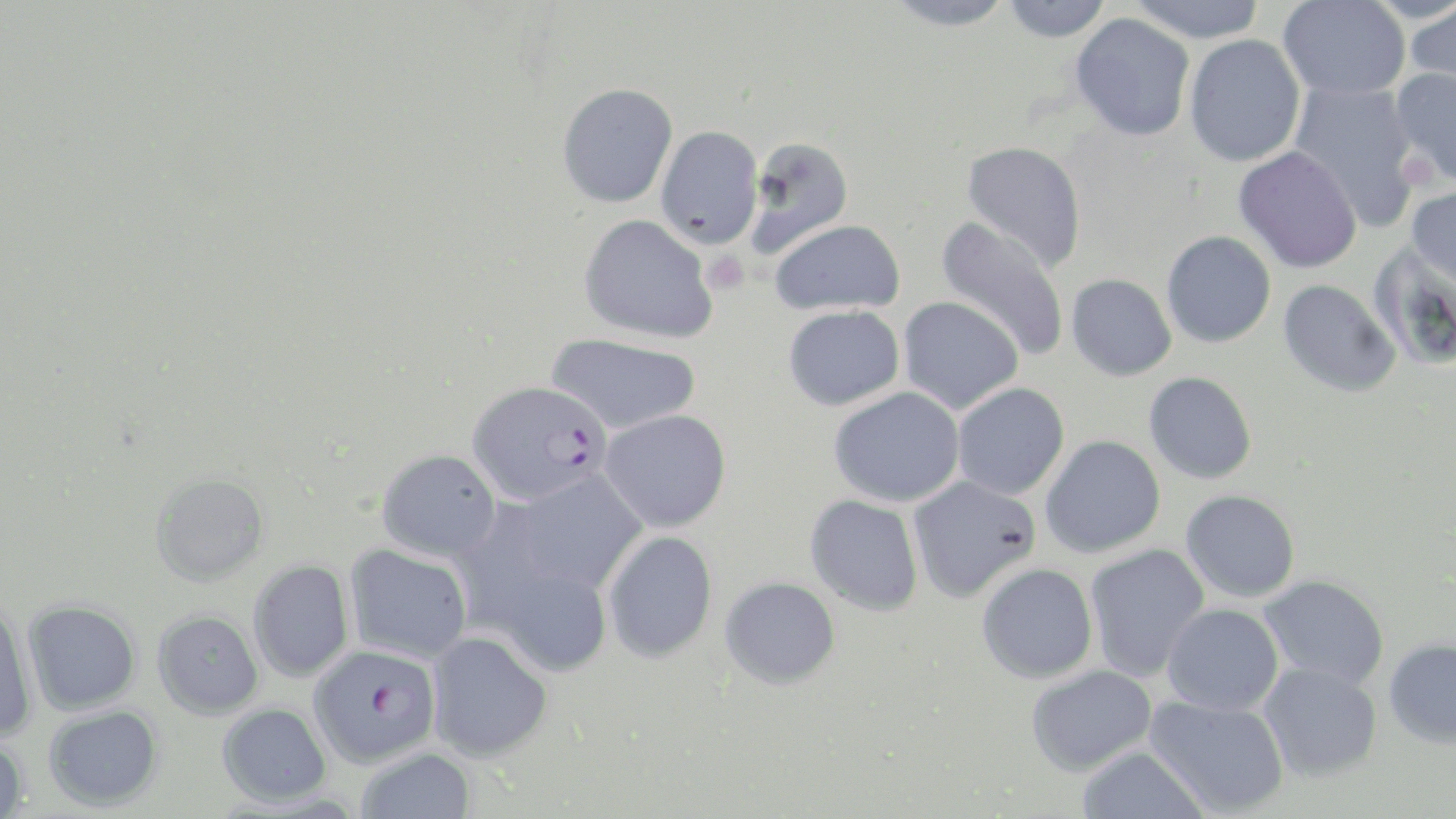

{
  "slide_level_diagnosis": "Plasmodium falciparum",
  "modality": "light microscopy",
  "uninfected_red_blood_cell_locations": "approximate bounding boxes as (x1,y1)-(x2,y2) corner pairs in pixels: (881,0)-(1016,31), (1001,0)-(1113,43), (1127,0)-(1268,43), (1277,0)-(1410,100), (1403,3)-(1456,97), (1069,13)-(1195,141), (1184,34)-(1305,167), (1391,67)-(1456,186), (1289,81)-(1422,229), (557,83)-(678,208), (655,126)-(764,249), (744,136)-(855,257), (961,140)-(1087,272), (1233,146)-(1363,273), (1407,184)-(1456,291), (578,214)-(717,343), (935,217)-(1070,362), (770,219)-(905,316), (1161,230)-(1276,348), (1367,242)-(1456,370), (1066,274)-(1177,381), (1278,279)-(1401,397), (898,296)-(1023,415), (783,305)-(904,410), (546,333)-(702,434), (1144,371)-(1257,484), (952,382)-(1070,500), (828,386)-(966,507), (600,409)-(731,533), (1040,435)-(1166,558), (377,449)-(502,560), (512,470)-(648,595), (150,472)-(270,587), (907,476)-(1041,603), (1181,489)-(1300,602), (805,494)-(924,616), (602,530)-(717,662), (344,544)-(472,664), (1084,544)-(1209,682), (479,555)-(614,677), (248,560)-(354,682), (977,563)-(1098,683), (1258,575)-(1390,689), (720,576)-(840,689), (0,598)-(39,743), (22,600)-(141,715), (1162,603)-(1284,716), (152,609)-(264,720), (425,631)-(553,761), (1383,637)-(1456,748), (1259,663)-(1382,782), (1025,665)-(1157,775), (1144,695)-(1289,817), (217,703)-(332,807), (43,705)-(163,811), (0,735)-(30,818), (1074,745)-(1210,818), (355,748)-(475,819)",
  "plasmodium_falciparum_infected_red_blood_cell_locations": "approximate bounding boxes as (x1,y1)-(x2,y2) corner pairs in pixels: (468,380)-(610,505), (309,643)-(441,767)",
  "preparation": "thin blood film",
  "magnification": "1000x",
  "image_size": "1456×819 pixels",
  "stain": "May-Grünwald-Giemsa",
  "platelet_locations": "approximate bounding boxes as (x1,y1)-(x2,y2) corner pairs in pixels: (1402,153)-(1439,186), (702,250)-(749,295)",
  "field_of_view": "single"
}